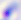
Summary:
  - Modality: micrograph
  - Magnification: 400x
  - Identification: Toxoplasma gondii